Locate every blood parasite and identify its species.
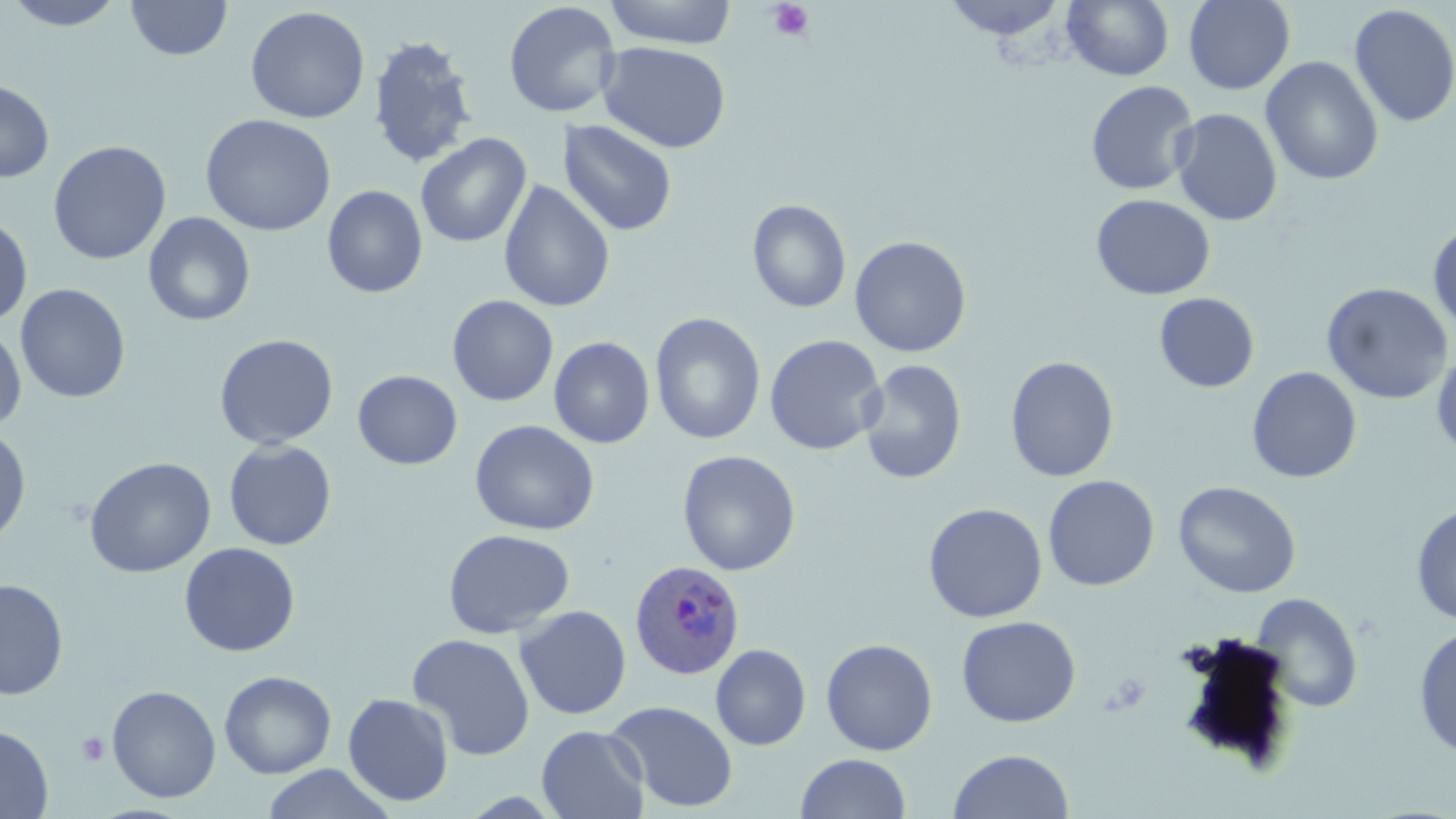
Approximate bounding boxes as [x1, y1, x2, y2] in pixels.
Plasmodium ovale-infected red blood cells: [629, 559, 744, 680].
No Plasmodium falciparum, Plasmodium malariae, Plasmodium vivax, Babesia divergens, or Trypanosoma brucei observed.

Platelet locations: [768, 1, 815, 42], [1106, 671, 1152, 715], [76, 733, 109, 765]. Uninfected red blood cell locations: [2, 0, 131, 31], [126, 0, 232, 61], [602, 0, 737, 48], [942, 0, 1068, 40], [1062, 0, 1174, 81], [1183, 0, 1295, 95], [502, 2, 621, 119], [1349, 4, 1456, 128], [245, 6, 370, 124], [367, 34, 479, 169], [598, 42, 731, 153], [1261, 55, 1384, 186], [0, 79, 55, 183], [1086, 80, 1199, 195], [1170, 108, 1282, 227], [200, 113, 337, 236], [557, 119, 677, 237], [415, 133, 531, 247], [48, 140, 171, 266], [498, 180, 615, 312], [322, 185, 428, 298], [1091, 193, 1216, 300], [747, 199, 851, 313], [142, 212, 256, 326], [0, 214, 33, 326], [1428, 222, 1456, 336], [849, 235, 972, 358], [1321, 282, 1454, 404], [14, 283, 131, 403], [1154, 292, 1259, 392], [447, 296, 558, 406], [650, 312, 766, 445], [0, 321, 27, 433], [214, 333, 339, 450], [764, 334, 886, 455], [549, 336, 655, 448], [1431, 348, 1456, 458], [1005, 356, 1120, 482], [858, 359, 967, 485], [1246, 367, 1362, 483], [352, 370, 463, 469], [470, 419, 599, 536], [0, 425, 31, 547], [223, 440, 337, 550], [677, 450, 801, 576], [84, 457, 216, 578], [1043, 474, 1160, 591], [1173, 480, 1301, 598], [922, 502, 1048, 623], [1411, 503, 1456, 626], [443, 529, 575, 639], [178, 541, 301, 657], [0, 577, 69, 700], [1250, 592, 1364, 713], [514, 605, 632, 720], [956, 615, 1081, 727], [1413, 624, 1456, 759], [407, 633, 535, 760], [820, 638, 938, 756], [710, 643, 811, 751], [219, 671, 336, 779], [106, 685, 221, 803], [342, 692, 454, 807], [607, 700, 738, 813], [0, 724, 53, 818], [536, 725, 650, 818], [947, 749, 1075, 819], [795, 753, 912, 819], [262, 764, 395, 819]. Slide-level diagnosis: Plasmodium ovale. 1000x magnification. Thin blood film. Image is 1456×819 pixels. May-Grünwald-Giemsa stain. Optical microscopy. One field of a larger specimen.